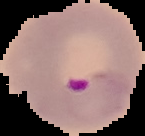

image_size: 145×136 pixels
preparation: thin blood film
image_type: segmented cell region on a black background
result: Plasmodium parasites detected